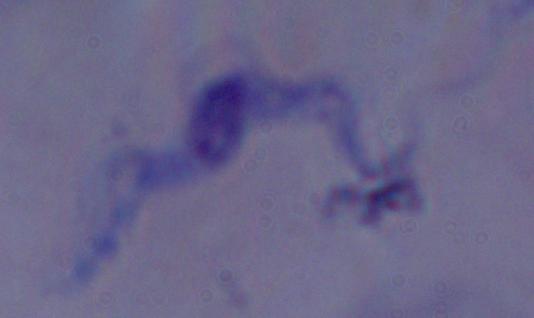

1000x magnification. Micrograph. A trypanosome is shown.